Describe the morphology of the red blood cells.
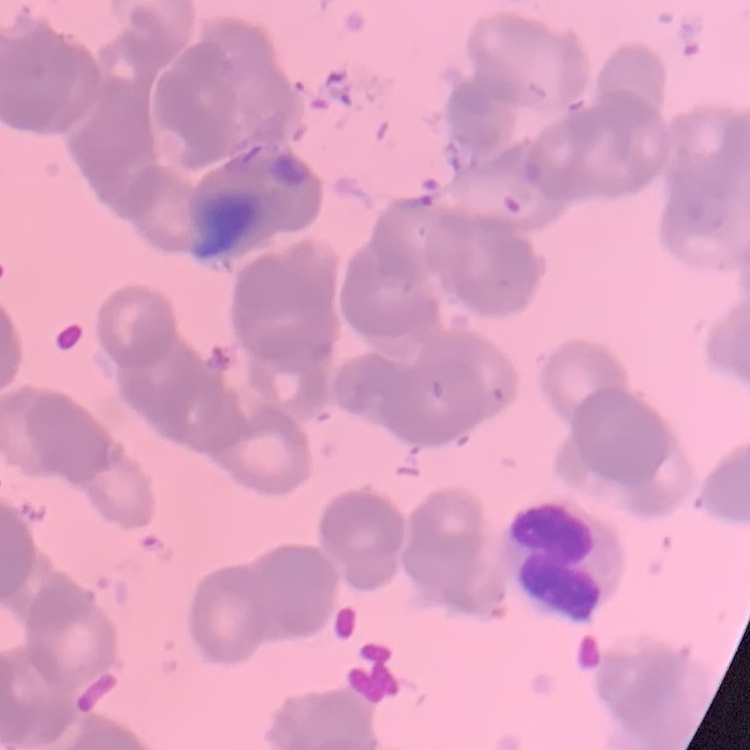

Rouleaux formation.

Summary:
  - Image type: square crop of a larger photomicrograph
  - Preparation: thin blood film
  - Stain: Field's or Giemsa